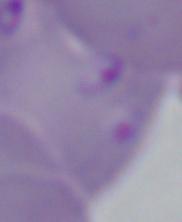

Summary:
  - Modality: photomicrograph
  - Identification: Babesia
  - Magnification: 1000x